Outline each uninfected red blood cell.
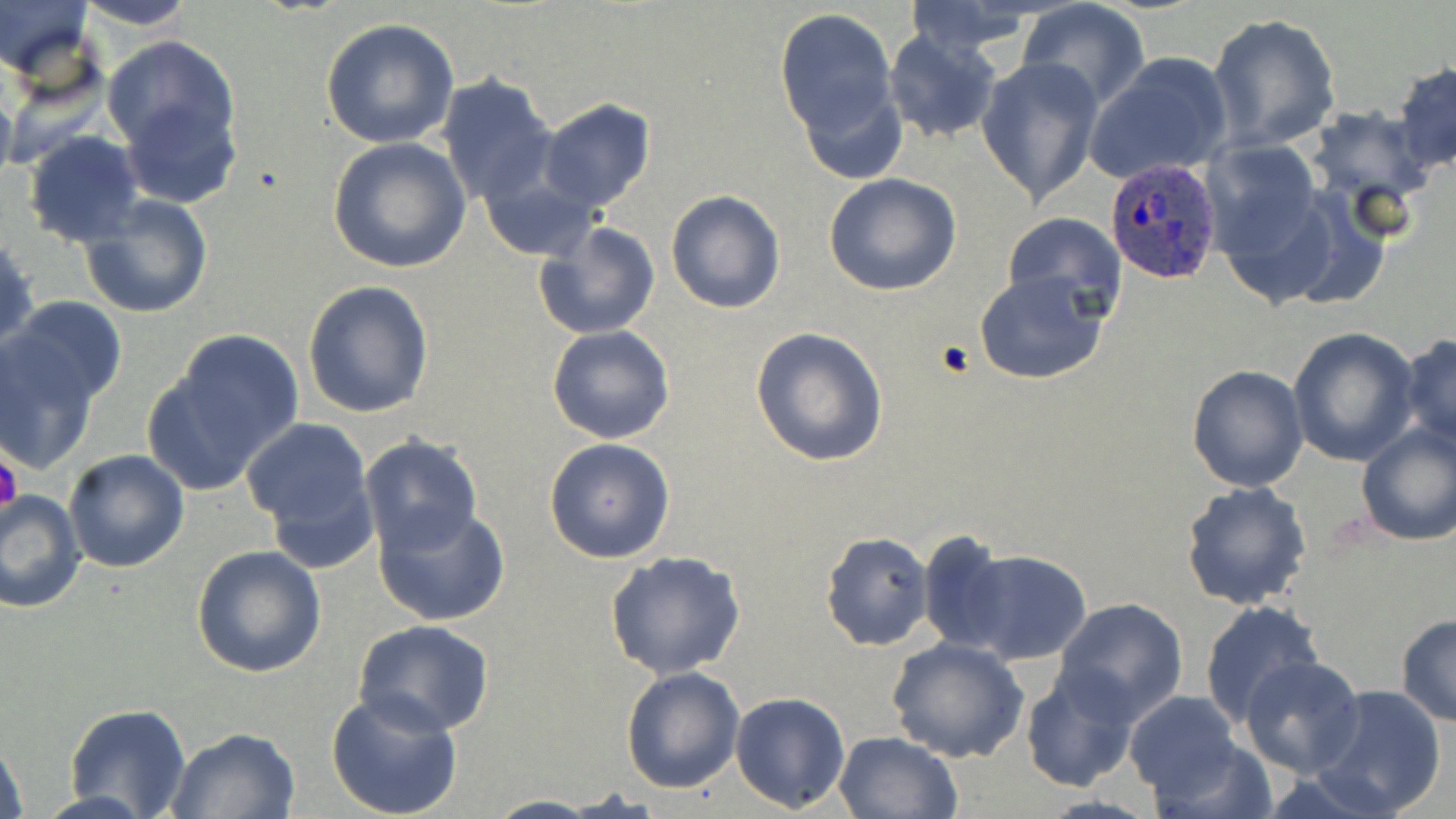
Approximate bounding boxes as (x1, y1, x2, y2) in pixels.
Uninfected red blood cells: (0, 0, 95, 90), (75, 0, 199, 31), (901, 0, 1046, 59), (1017, 1, 1151, 111), (774, 7, 899, 140), (1206, 12, 1343, 150), (319, 18, 461, 149), (882, 31, 1002, 146), (100, 33, 242, 178), (1086, 53, 1236, 185), (976, 56, 1104, 207), (1391, 62, 1456, 173), (435, 73, 558, 208), (796, 79, 911, 182), (538, 98, 656, 212), (1305, 105, 1437, 211), (22, 131, 147, 247), (328, 138, 471, 273), (1203, 140, 1326, 267), (824, 173, 963, 295), (481, 174, 595, 259), (665, 189, 786, 314), (77, 194, 213, 321), (1001, 211, 1127, 320), (534, 221, 660, 341), (0, 234, 38, 353), (974, 271, 1110, 384), (302, 279, 435, 419), (5, 296, 128, 412), (546, 325, 677, 444), (750, 327, 890, 467), (1287, 328, 1421, 467), (150, 332, 301, 487), (1399, 333, 1456, 449), (0, 335, 103, 474), (1187, 365, 1308, 492), (241, 417, 374, 544), (1354, 420, 1456, 546), (358, 434, 484, 558), (542, 437, 675, 564), (63, 448, 191, 573), (1180, 482, 1314, 612), (1, 490, 86, 613), (374, 502, 512, 627), (819, 530, 935, 650), (918, 530, 1017, 654), (190, 545, 325, 680), (949, 546, 1092, 666), (605, 552, 748, 680), (1053, 597, 1189, 721), (1199, 599, 1325, 727), (1396, 615, 1456, 726), (354, 619, 495, 735), (885, 636, 1030, 762), (1239, 653, 1366, 776), (1020, 665, 1142, 791), (620, 666, 744, 793), (1313, 684, 1448, 817), (324, 690, 465, 819), (731, 691, 851, 811), (1123, 691, 1243, 803), (65, 704, 193, 819), (165, 727, 300, 817), (833, 731, 964, 819), (0, 733, 30, 819), (1151, 736, 1279, 818), (482, 795, 608, 819).

slide-level diagnosis = Plasmodium ovale
stain = May-Grünwald-Giemsa
magnification = 1000x
image size = 1456×819 pixels
platelet locations = approximate bounding boxes as (x1, y1, x2, y2) in pixels: (935, 340, 976, 378), (0, 452, 24, 516)
Plasmodium ovale-infected red blood cell locations = approximate bounding boxes as (x1, y1, x2, y2) in pixels: (1100, 153, 1222, 281)
field of view = one of a larger specimen
modality = optical microscopy
preparation = thin blood smear